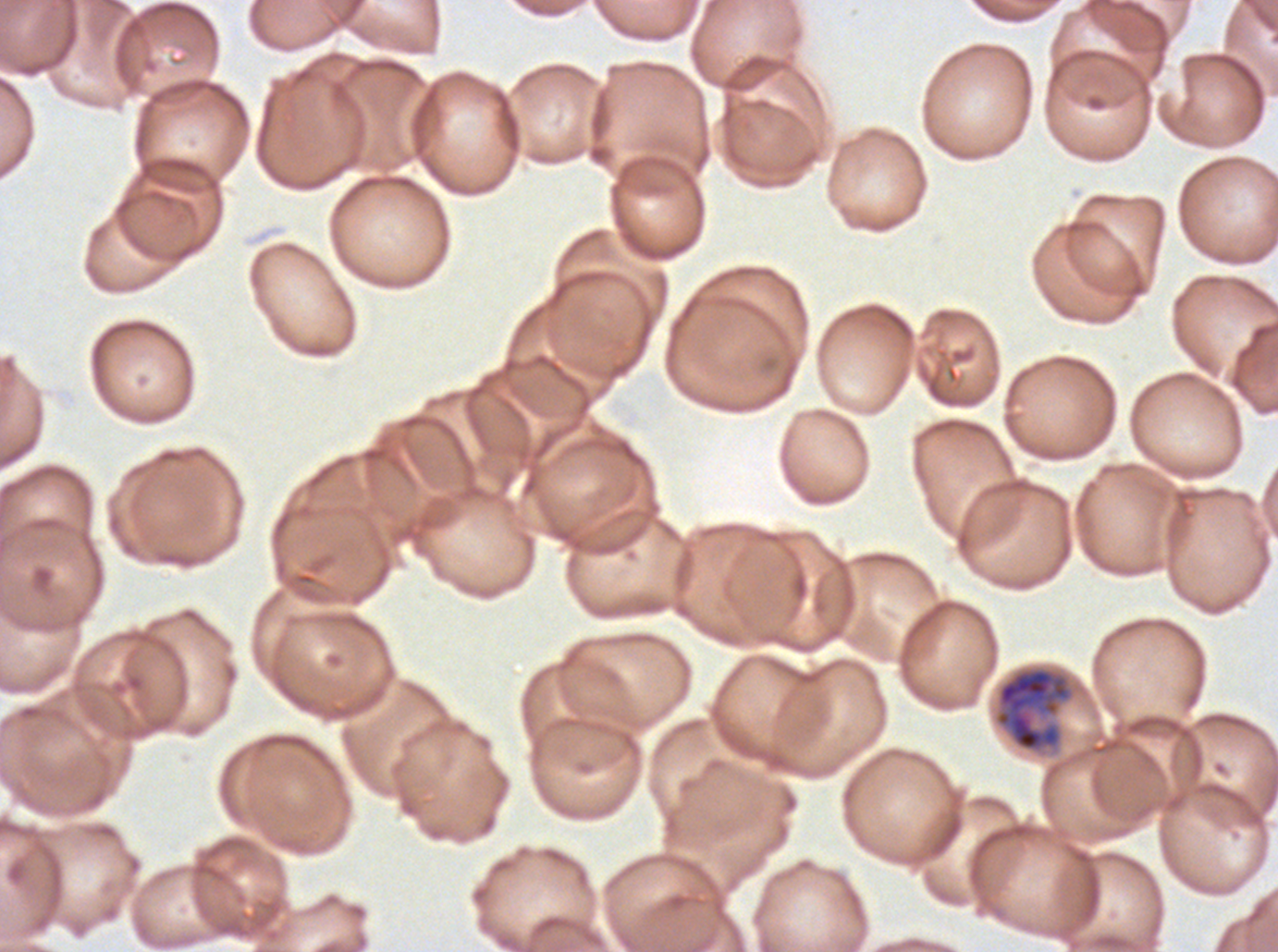

notation = approximate bounding rectangles given as corner coordinates in pixels from the top-left
late schizont locations = (x1=992, y1=665, x2=1076, y2=755)
specimen = Plasmodium falciparum from a patient in The Gambia, cultured ex vivo for 24 to 48 hours
image size = 1278×952 pixels
stain = Giemsa
preparation = thin blood smear
field of view = one sub-image of a larger composite